Give the position of every leukocyte visible.
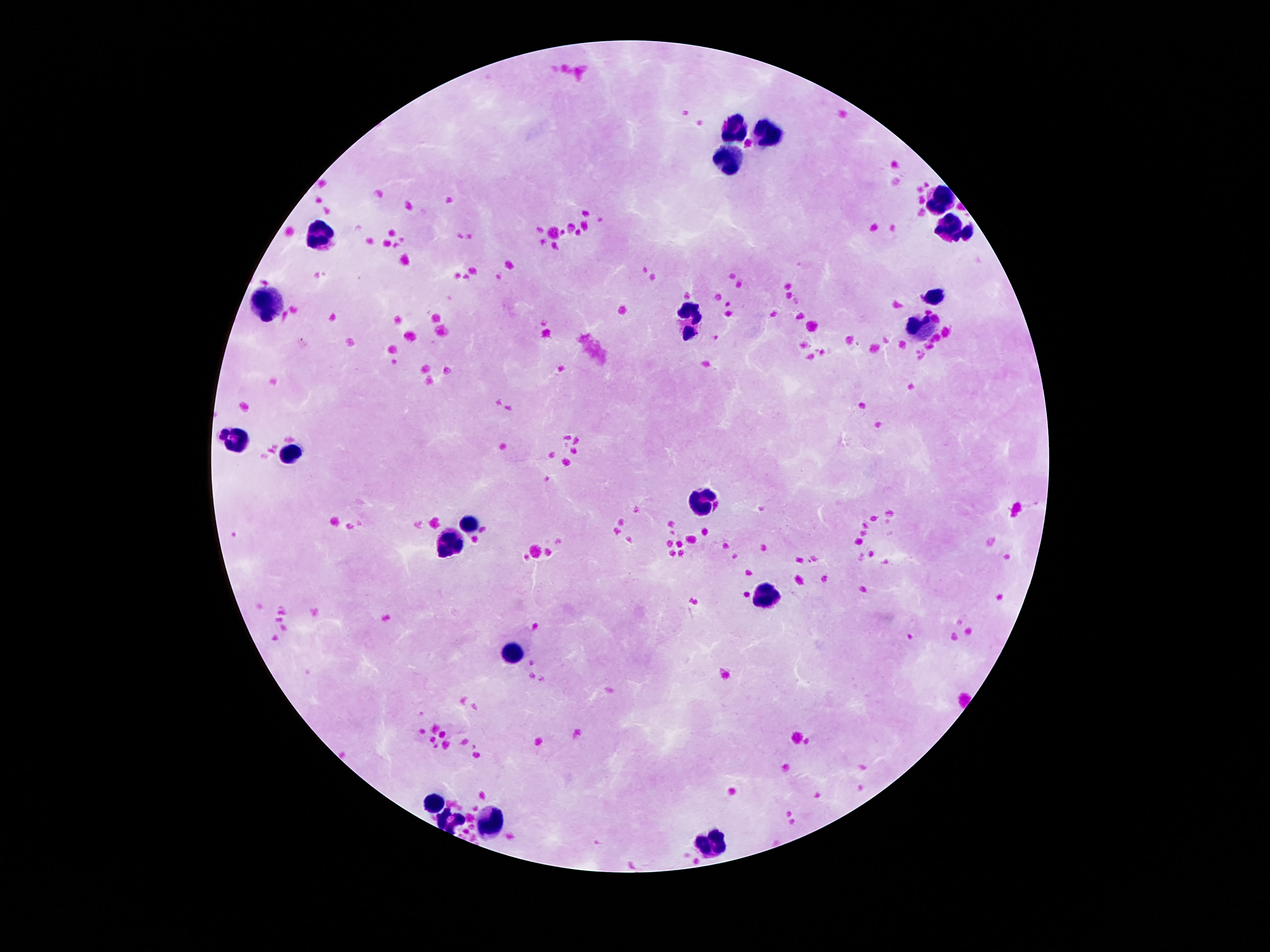

Approximate centers as [x, y] in pixels.
Leukocytes: [737, 127], [769, 130], [727, 160], [939, 200], [950, 227], [320, 232], [935, 296], [269, 302], [693, 321], [916, 326], [234, 438], [292, 449], [704, 500], [469, 521], [448, 544], [765, 594], [511, 652], [435, 805], [448, 819], [490, 822], [712, 843].

Thick blood film. Patient malaria status: negative. 100x magnification. Smartphone photograph taken through the microscope eyepiece. Image is 1270×952 pixels. Giemsa stain. One field from this slide.